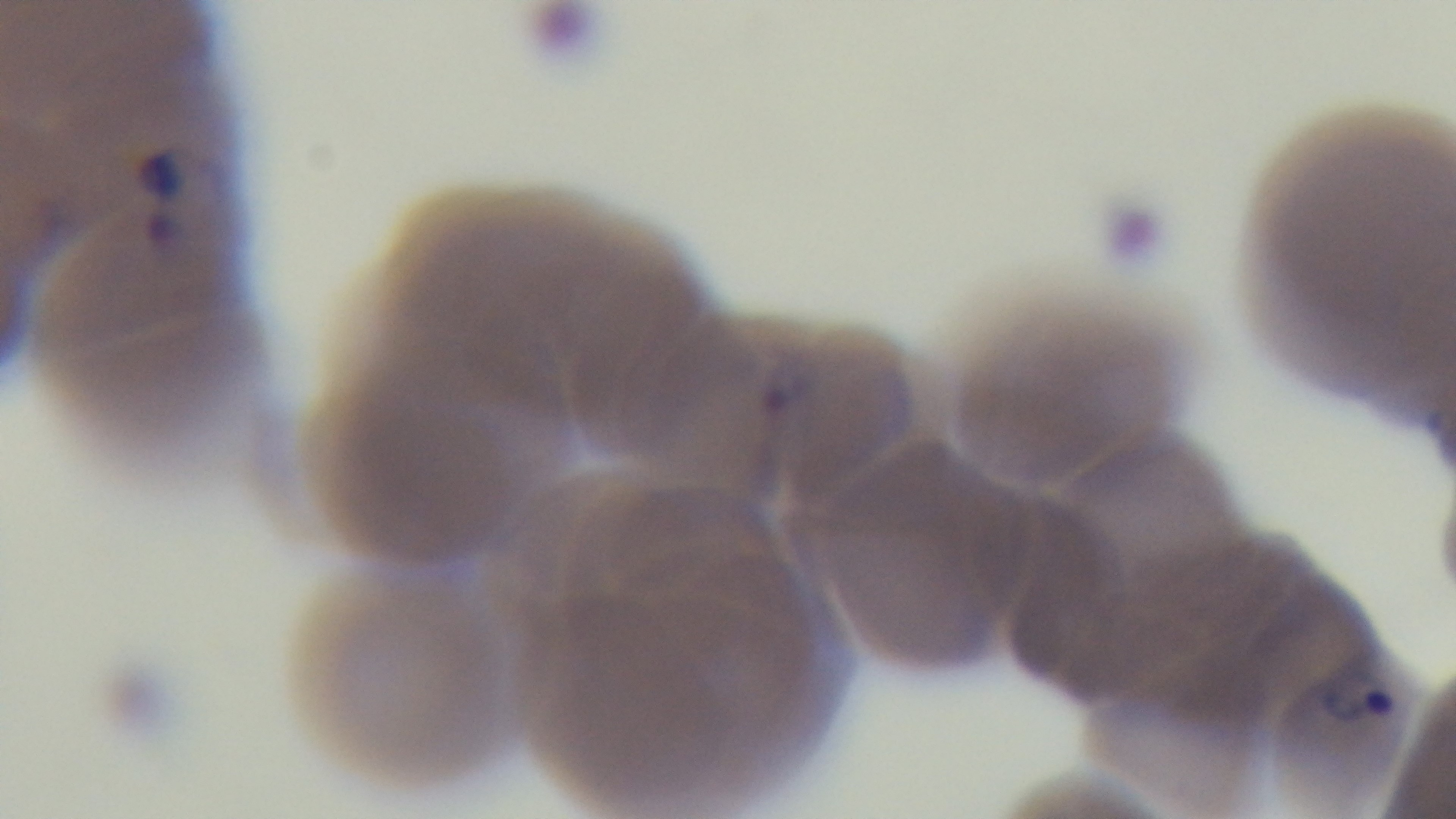
modality = light microscopy
objective = 100x oil immersion
capture = mounted 4K digital camera
preparation = thin blood film
stain = Giemsa
field of view = one from the slide
malaria status = infected